Identify the cell.
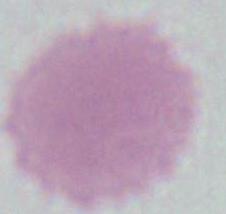
This is an erythrocyte.

Photomicrograph. 1000x magnification.